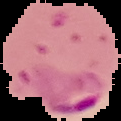
Summary:
  - Image size: 121×121 pixels
  - Image type: segmented cell region with the area outside set to black
  - Preparation: thin blood film
  - Result: Plasmodium parasites detected